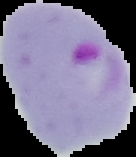
Summary:
  - Preparation: thin blood film
  - Malaria status: parasitized
  - Image type: segmented cell region on a black background
  - Image size: 136×157 pixels